Identify the cell.
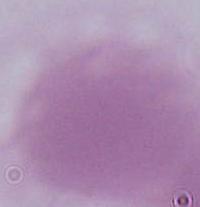

This is an erythrocyte.

Summary:
  - Modality: photomicrograph
  - Magnification: 1000x